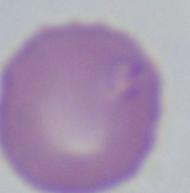 A Babesia parasite is seen. Captured at 1000x magnification. Micrograph.